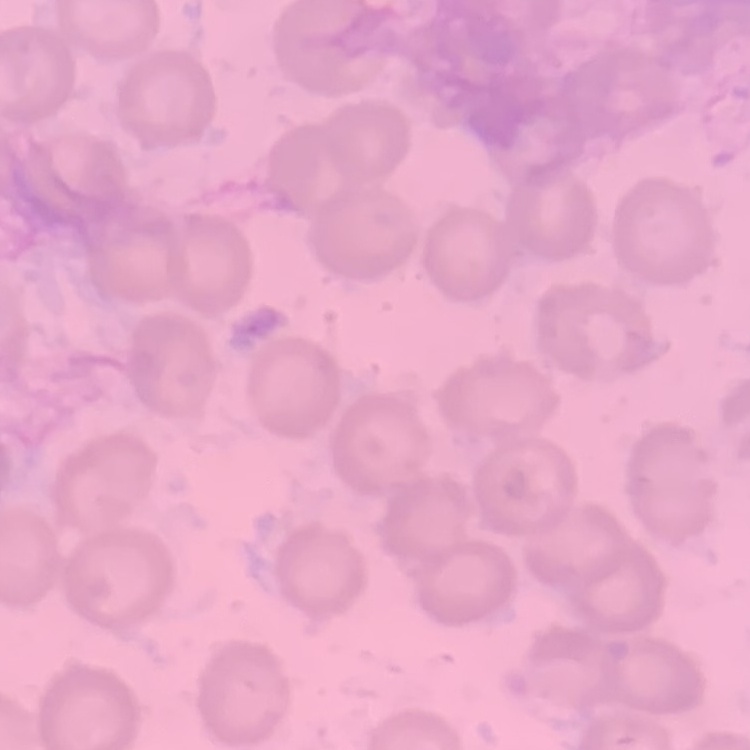

erythrocyte morphology = no rouleaux formation
preparation = thin blood film
image type = square crop of a larger photomicrograph
stain = Field's or Giemsa